Report the malaria status of this cell.
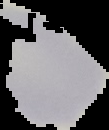
Uninfected.

From a thin blood smear. Image is 109×130 pixels. Segmented cell region on a black background.